Report the malaria status of this cell.
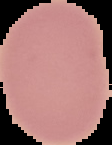
It is uninfected.

image_type: cell region segmented out of the field of view; surrounding area masked to black
image_size: 112×145 pixels
preparation: thin blood smear